Classify this cell by malaria status.
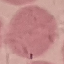

Uninfected.

{
  "image_type": "cell patch, automatically extracted from a larger field of view and resized to 64 × 64 pixels",
  "capture": "smartphone camera at the microscope eyepiece",
  "preparation": "thin blood film",
  "stain": "Giemsa"
}